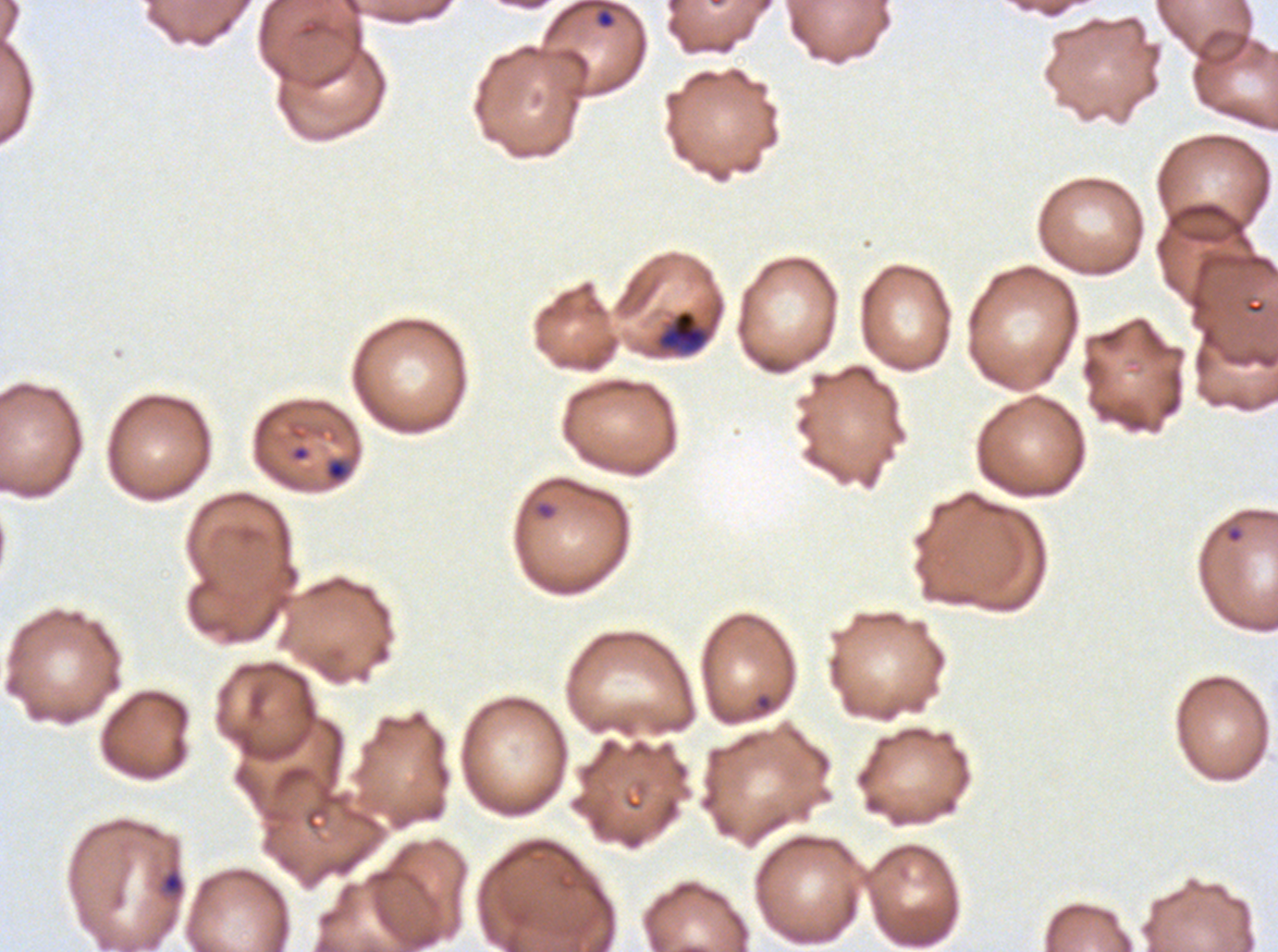

life_cycle_stages_observed: ring, late-ring/early-trophozoite
ring_locations: 'approximate bounding rectangles given as corner coordinates in pixels from the top-left: (x1=596, y1=8, x2=616, y2=30), (x1=325, y1=458, x2=350, y2=482), (x1=535, y1=501, x2=556, y2=519), (x1=1223, y1=523, x2=1246, y2=545), (x1=755, y1=693, x2=773, y2=713), (x1=160, y1=868, x2=185, y2=896)'
preparation: thin blood film
field_of_view: sub-image separated from a larger composite
stain: Giemsa
late_ring_early_trophozoite_locations: 'approximate bounding rectangles given as corner coordinates in pixels from the top-left: (x1=658, y1=310, x2=707, y2=353)'
image_size: 1278×952 pixels
specimen: P. falciparum from a patient in The Gambia, cultured ex vivo for 24 to 48 hours